Identify the parasite.
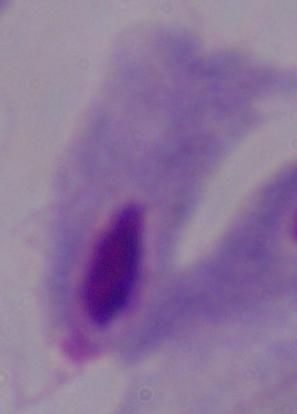

This is a trichomonad.

1000x magnification. Photomicrograph.